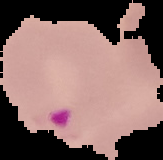

image size = 163×160 pixels
image type = segmented cell region with the area outside set to black
result = malaria parasites detected
preparation = thin blood film